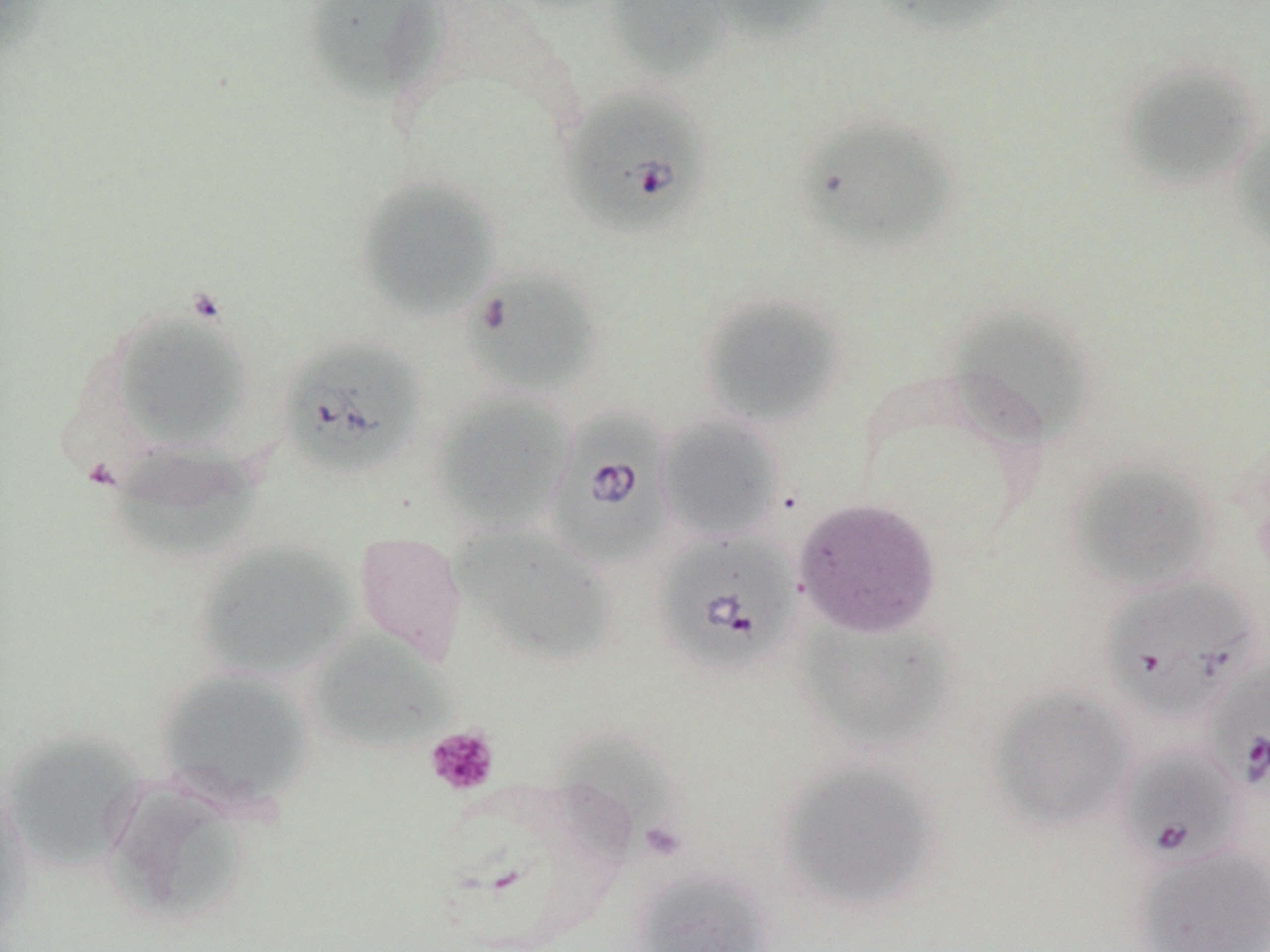

Summary:
  - Coordinate format: approximate bounding boxes as (x1, y1, x2, y2) in pixels
  - Uninfected red blood cell locations: (302, 0, 447, 108), (604, 0, 727, 80), (702, 0, 835, 43), (868, 1, 1029, 38), (1118, 63, 1261, 188), (797, 114, 959, 250), (1229, 125, 1270, 256), (353, 174, 502, 322), (463, 270, 601, 397), (698, 293, 845, 427), (949, 306, 1092, 445), (111, 313, 252, 450), (432, 393, 574, 534), (656, 415, 783, 542), (101, 443, 266, 561), (1067, 458, 1219, 594), (794, 498, 941, 639), (452, 522, 616, 665), (353, 531, 468, 664), (195, 541, 357, 681), (794, 620, 956, 753), (309, 631, 457, 754), (154, 668, 315, 812), (988, 685, 1136, 831), (1, 728, 148, 872), (552, 732, 680, 861), (777, 758, 941, 913), (103, 780, 252, 928), (0, 785, 37, 942), (1134, 845, 1270, 952), (632, 870, 774, 952)
  - Platelet locations: (425, 725, 500, 796)
  - Babesia divergens-infected red blood cell locations: (560, 88, 711, 237), (278, 336, 426, 477), (543, 408, 677, 571), (652, 529, 801, 677), (1099, 575, 1261, 722), (1205, 652, 1270, 794), (1117, 745, 1243, 871)
  - Slide-level diagnosis: Babesia divergens
  - Modality: optical microscopy
  - Stain: May-Grünwald-Giemsa
  - Preparation: thin blood film
  - Field of view: single
  - Magnification: 1000x
  - Image size: 1270×952 pixels